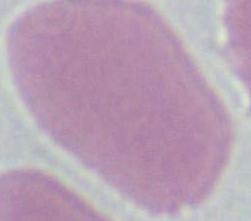
Summary:
  - Modality: photomicrograph
  - Identification: red blood cell
  - Magnification: 1000x